Give the position of every malaria parasite.
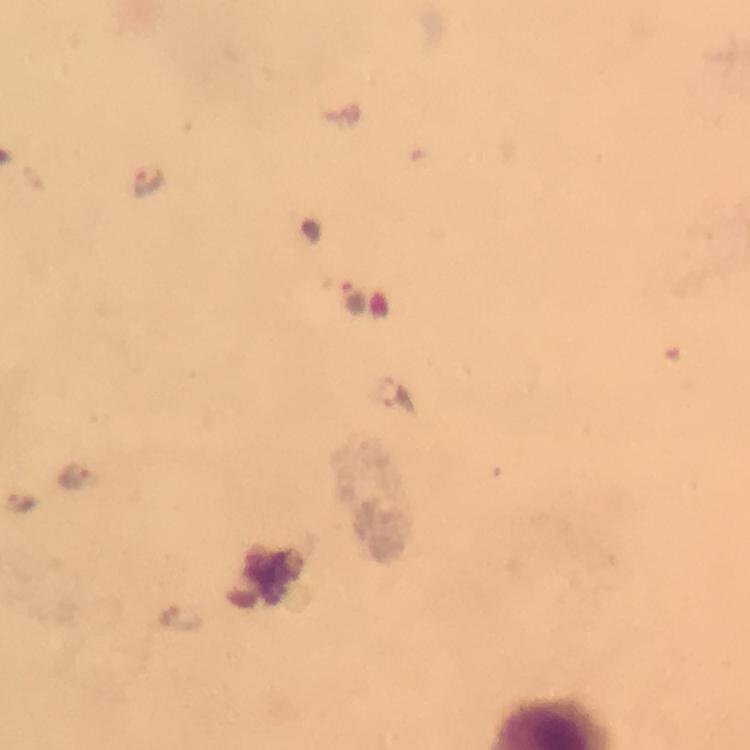
Approximate centers as (x, y) in pixels.
Malaria parasites: (149, 177), (352, 298), (76, 479), (24, 506), (176, 614).

Image is 750×750 pixels. Giemsa stain. Thick blood smear. Immersion oil was used. From a diagnostic examination for malaria. Photographed through the microscope with a smartphone camera. A crop from one field of view. 100x magnification.